Point out each malaria parasite.
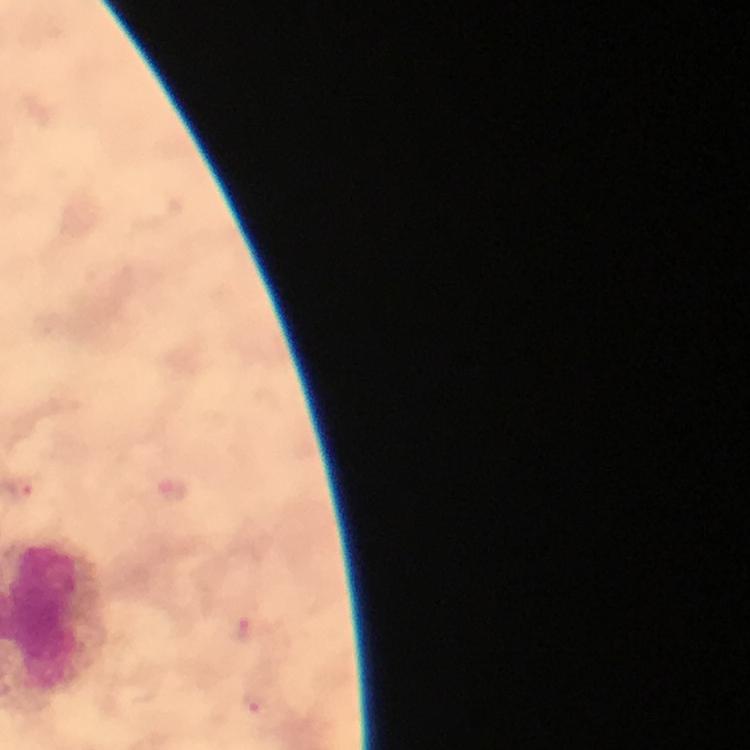

Approximate centers as {x, y} in pixels.
Malaria parasites: {24, 487}, {240, 628}, {256, 707}.

{
  "magnification": "100x",
  "stain": "Giemsa",
  "image_size": "750×750 pixels",
  "context": "from a malaria diagnostic workup",
  "capture": "smartphone camera through the microscope",
  "immersion_oil": "used",
  "preparation": "thick smear",
  "cropped_from": "a single field of view"
}